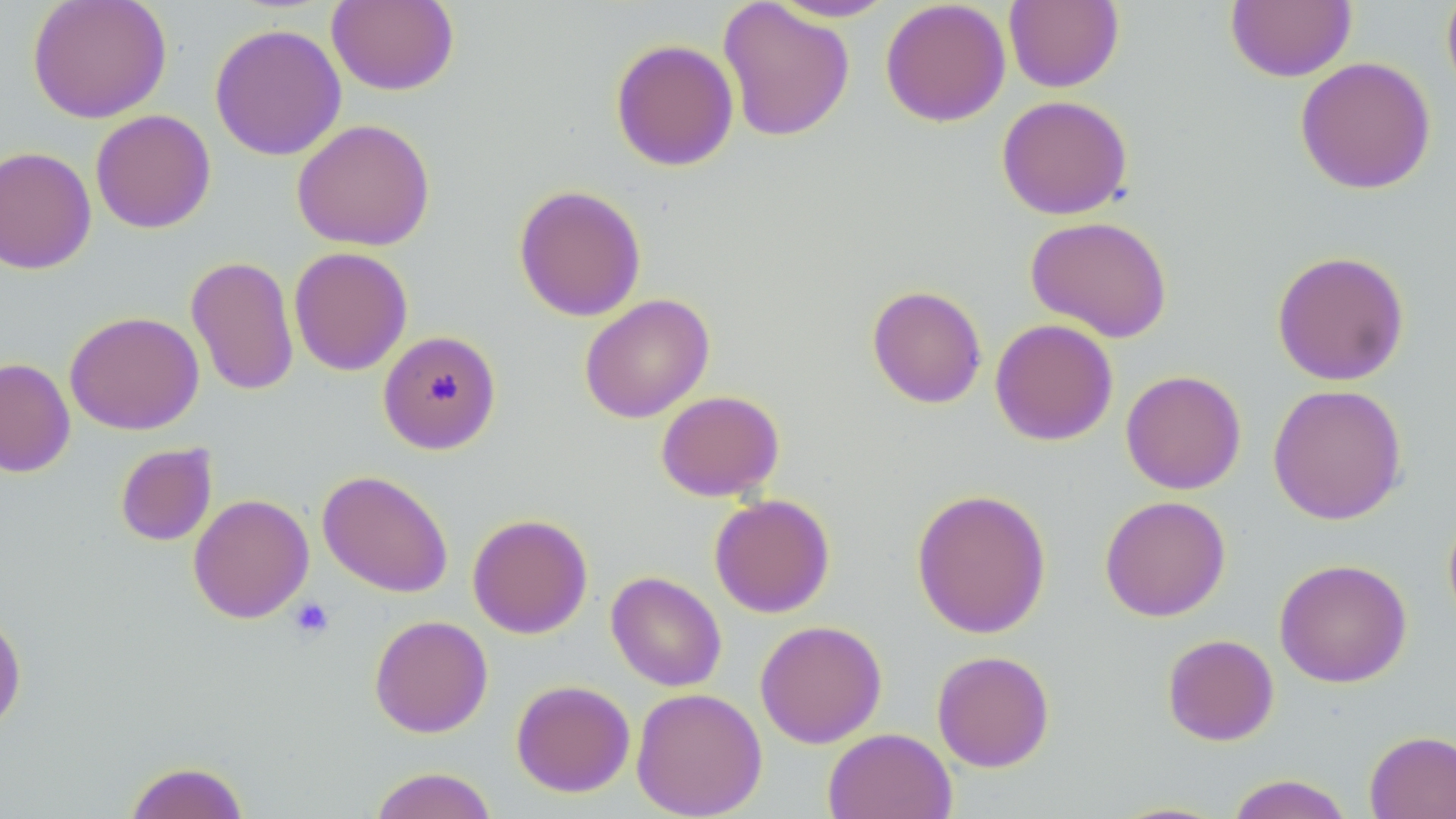

Summary:
  - Coordinate format: approximate bounding boxes as [x1, y1, x2, y2] in pixels
  - Uninfected red blood cell locations: [27, 0, 172, 123], [767, 0, 899, 22], [880, 0, 1010, 127], [1225, 0, 1357, 82], [1441, 0, 1456, 101], [327, 1, 459, 95], [717, 1, 855, 142], [1004, 1, 1124, 92], [209, 23, 347, 161], [610, 38, 739, 172], [1294, 56, 1437, 195], [996, 94, 1133, 220], [90, 109, 216, 234], [291, 118, 435, 251], [0, 146, 96, 275], [513, 184, 646, 322], [1025, 215, 1172, 342], [288, 246, 413, 376], [1271, 250, 1410, 386], [185, 255, 300, 396], [866, 284, 987, 409], [579, 293, 715, 423], [64, 311, 204, 435], [990, 318, 1118, 446], [378, 330, 502, 455], [0, 358, 76, 478], [1120, 369, 1246, 494], [1267, 383, 1407, 525], [655, 390, 784, 502], [114, 442, 217, 547], [317, 469, 453, 597], [911, 488, 1052, 639], [188, 493, 314, 623], [709, 494, 835, 618], [1099, 495, 1231, 622], [1442, 507, 1456, 634], [467, 513, 593, 639], [1274, 558, 1412, 688], [606, 571, 727, 691], [0, 607, 27, 736], [369, 614, 493, 738], [755, 619, 887, 748], [1162, 633, 1279, 746], [932, 650, 1055, 772], [510, 680, 635, 797], [630, 687, 767, 818], [823, 727, 957, 819], [1364, 729, 1456, 818], [122, 760, 251, 819], [368, 766, 500, 819], [1224, 774, 1356, 819]
  - Platelet locations: [288, 597, 334, 640]
  - Slide-level diagnosis: no evidence of blood parasites
  - Magnification: 1000x
  - Modality: light microscopy
  - Preparation: thin blood film
  - Image size: 1456×819 pixels
  - Stain: May-Grünwald-Giemsa
  - Field of view: single